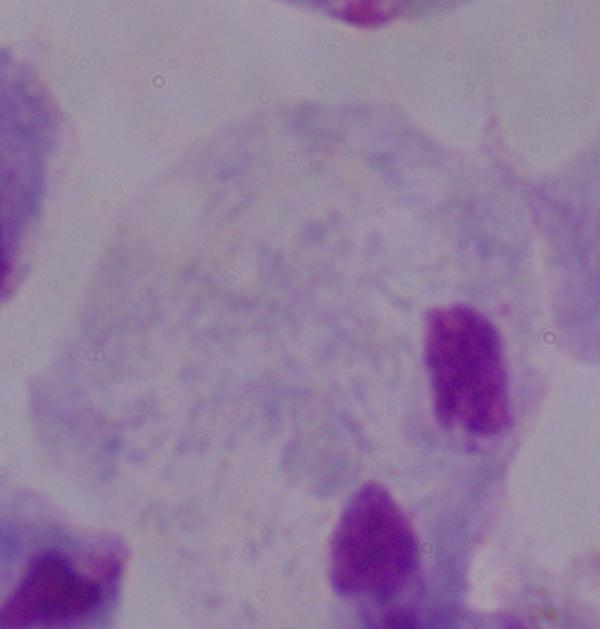
A trichomonad is seen. Photomicrograph. 1000x magnification.